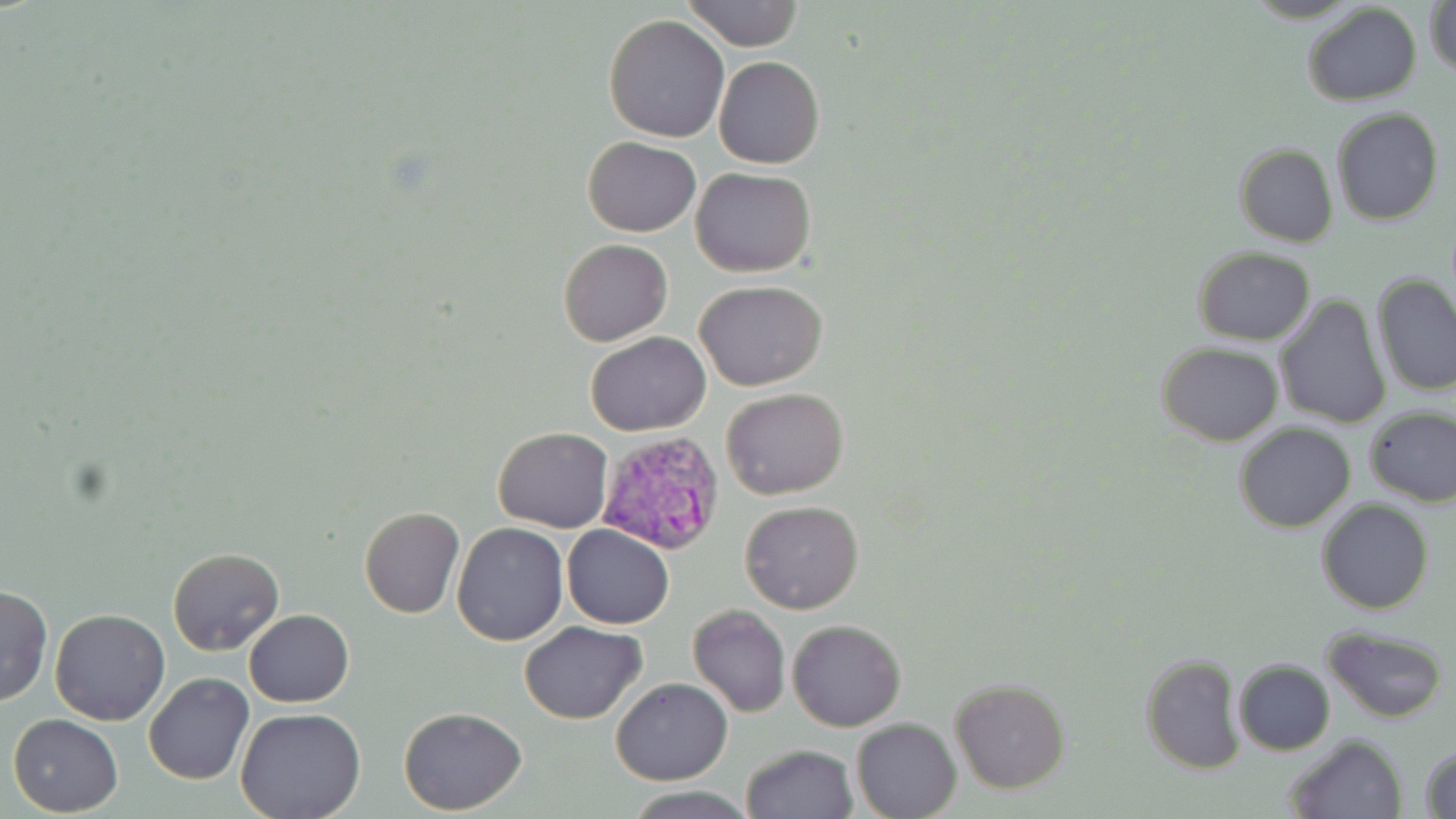

Summary:
  - Coordinate format: approximate bounding boxes as (x1, y1, x2, y2) in pixels
  - Plasmodium vivax-infected red blood cell locations: (596, 429, 725, 554)
  - Uninfected red blood cell locations: (681, 0, 805, 51), (1426, 0, 1456, 80), (1301, 4, 1422, 106), (603, 15, 730, 141), (714, 57, 825, 170), (1332, 107, 1444, 226), (583, 135, 701, 237), (1234, 143, 1338, 247), (690, 167, 816, 277), (557, 239, 672, 347), (1192, 246, 1316, 345), (1371, 275, 1456, 396), (694, 279, 827, 391), (1275, 293, 1392, 432), (585, 332, 710, 436), (1157, 341, 1283, 446), (721, 386, 849, 499), (1363, 404, 1456, 507), (1233, 422, 1358, 533), (493, 426, 613, 531), (739, 499, 864, 614), (1317, 499, 1434, 616), (360, 506, 464, 618), (451, 521, 568, 646), (560, 524, 674, 629), (167, 546, 284, 656), (0, 584, 52, 707), (687, 605, 791, 717), (49, 608, 171, 726), (244, 610, 354, 707), (520, 620, 648, 724), (787, 620, 905, 731), (1322, 625, 1450, 724), (1139, 653, 1245, 774), (1232, 659, 1335, 755), (144, 672, 254, 785), (612, 678, 731, 785), (949, 678, 1070, 793), (398, 707, 527, 814), (235, 709, 365, 819), (8, 713, 123, 816), (851, 717, 960, 819), (1282, 734, 1406, 819), (741, 744, 857, 819), (1418, 744, 1456, 818), (623, 787, 756, 818)
  - Slide-level diagnosis: Plasmodium vivax
  - Stain: May-Grünwald-Giemsa
  - Field of view: single
  - Preparation: thin blood film
  - Magnification: 1000x
  - Modality: light microscopy
  - Image size: 1456×819 pixels